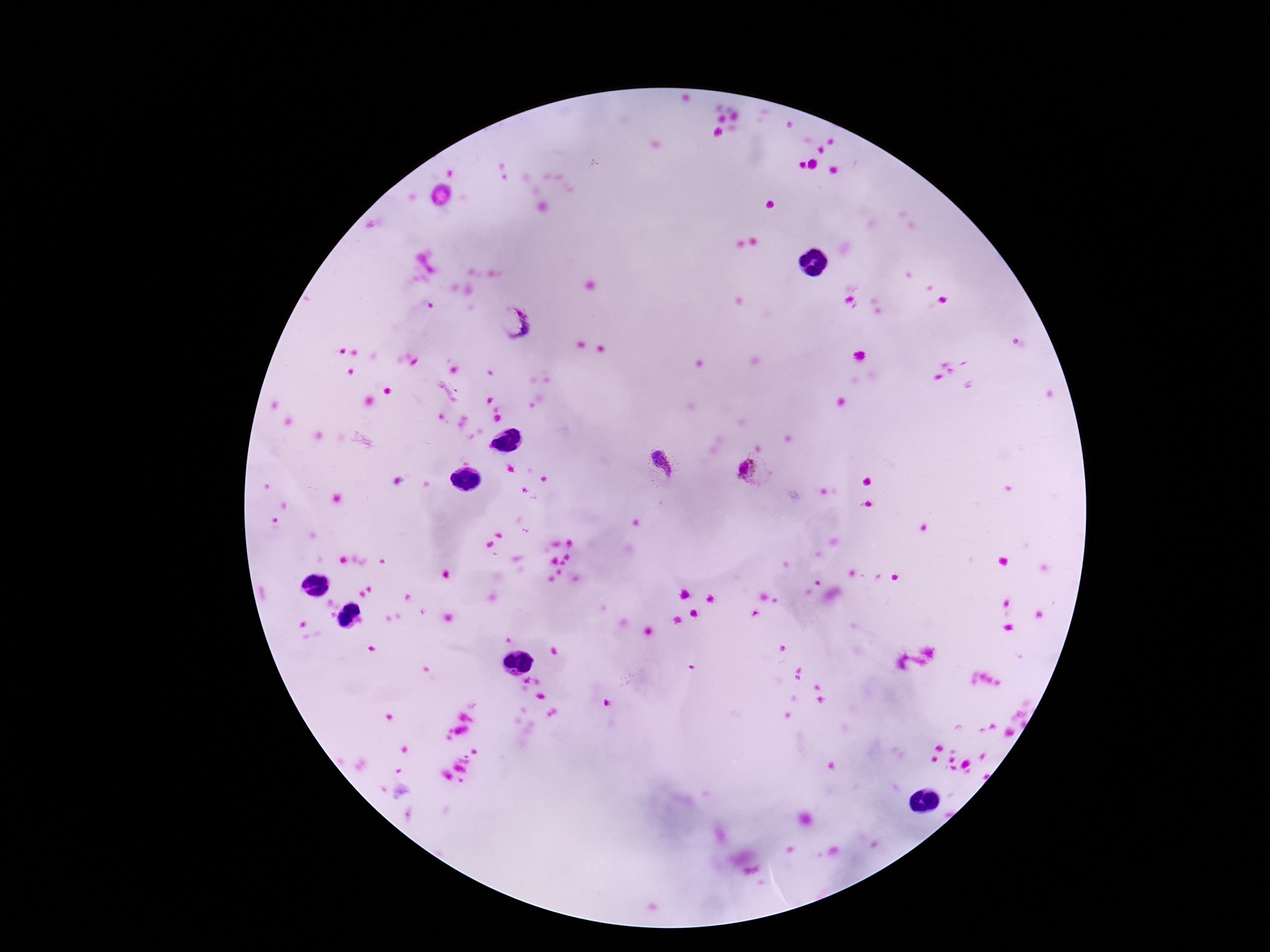

Approximate centers as {x, y} in pixels.
Summary:
  - Plasmodium parasite locations: {516, 321}, {660, 466}, {756, 472}
  - Field of view: one from this slide
  - Stain: Giemsa
  - Capture: smartphone camera through the microscope eyepiece
  - Patient malaria status: positive
  - Preparation: thick blood film
  - Image size: 1270×952 pixels
  - Magnification: 100x